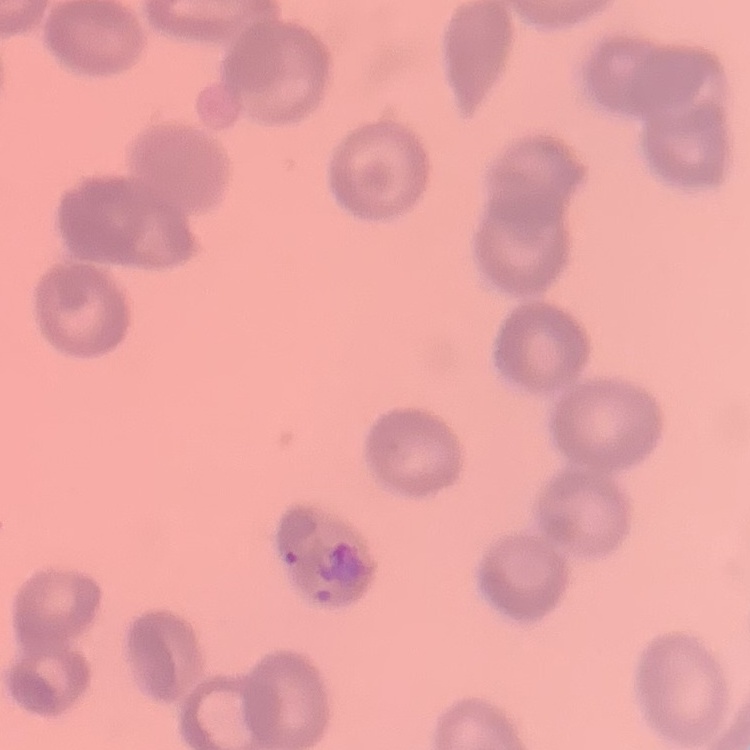

erythrocyte morphology = rouleaux formation
stain = Field's or Giemsa
preparation = thin blood film
image type = square crop of a larger photomicrograph